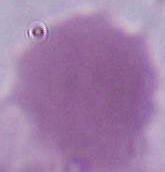

Summary:
  - Modality: photomicrograph
  - Magnification: 1000x
  - Identification: erythrocyte